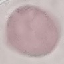

malaria_status: uninfected
stain: Giemsa
capture: smartphone through the microscope eyepiece
image_type: cell patch, automatically extracted from a larger field of view and resized to 64 × 64 pixels
preparation: thin smear